Evaluate for parasitized red blood cells.
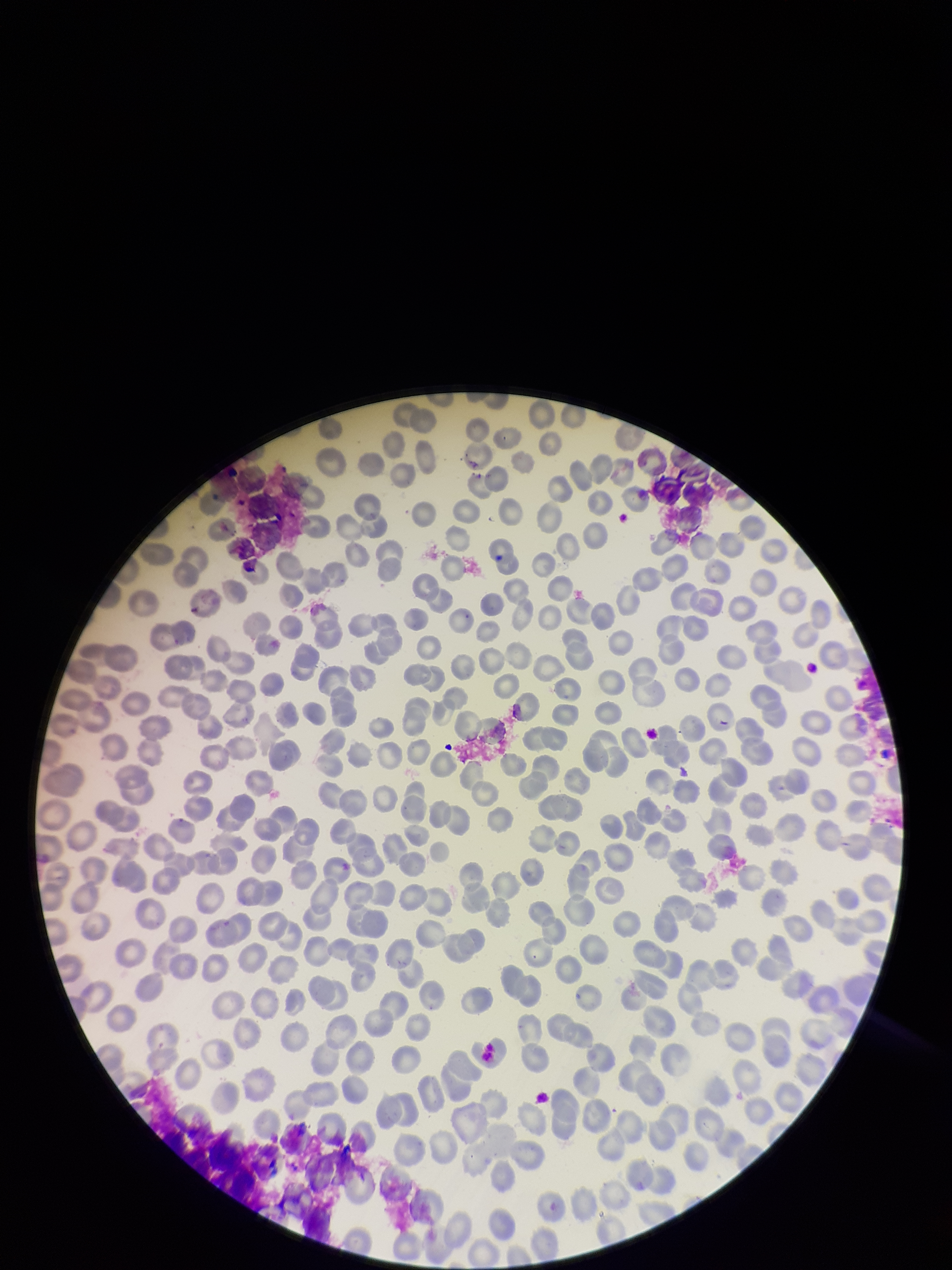

None seen.

Summary:
  - Parasitized red blood cell count: 0
  - Red blood cell count: 295
  - Field of view: one from this slide
  - Patient malaria status: negative
  - Image size: 952×1270 pixels
  - Preparation: thin blood smear
  - Stain: Giemsa
  - Capture: smartphone photograph through the microscope eyepiece